Give the extent of all Plasmodium falciparum-infected red blood cells.
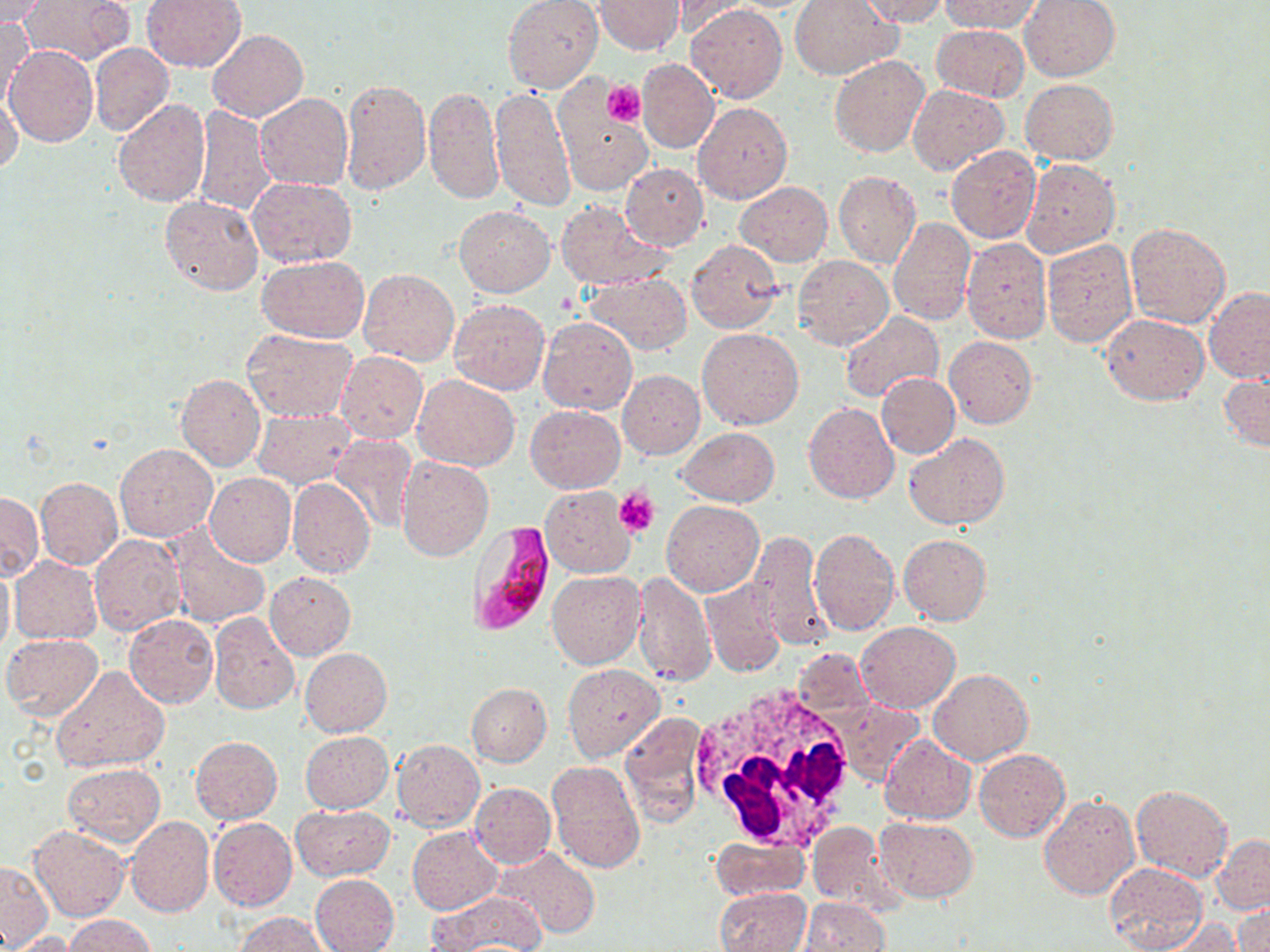
Approximate bounding boxes as (x1,y1)-(x2,y2) corner pairs in pixels.
Plasmodium falciparum-infected red blood cells: (466,520)-(556,636).

slide-level diagnosis = Plasmodium falciparum
white blood cell locations = approximate bounding boxes as (x1,y1)-(x2,y2) corner pairs in pixels: (690,683)-(859,855)
stain = May-Grünwald-Giemsa
uninfected red blood cell locations = approximate bounding boxes as (x1,y1)-(x2,y2) corner pairs in pixels: (21,0)-(135,65), (140,0)-(247,72), (503,0)-(603,93), (594,0)-(685,54), (789,0)-(900,79), (854,0)-(949,25), (941,0)-(1043,33), (1020,0)-(1120,81), (0,1)-(51,27), (669,2)-(747,39), (686,4)-(787,103), (0,18)-(34,110), (930,25)-(1029,102), (208,29)-(308,122), (90,42)-(174,137), (4,45)-(99,148), (830,54)-(928,157), (637,59)-(719,153), (1021,78)-(1118,165), (341,79)-(431,195), (490,85)-(576,211), (909,85)-(1010,174), (424,86)-(502,205), (0,91)-(22,170), (255,93)-(353,191), (113,98)-(211,207), (557,102)-(651,195), (693,102)-(792,204), (195,105)-(274,216), (945,147)-(1042,244), (1023,158)-(1121,259), (621,163)-(709,250), (834,171)-(921,269), (247,177)-(357,268), (736,181)-(833,267), (160,195)-(263,296), (556,200)-(669,289), (453,205)-(555,296), (888,217)-(977,324), (1125,222)-(1231,329), (961,238)-(1050,343), (687,239)-(784,333), (1041,239)-(1136,345), (257,254)-(370,341), (795,255)-(893,349), (358,269)-(459,365), (583,273)-(691,354), (1204,287)-(1270,384), (448,298)-(550,394), (839,311)-(943,405), (1101,313)-(1207,405), (539,317)-(637,415), (698,327)-(803,429), (244,328)-(356,422), (945,337)-(1037,429), (335,352)-(427,443), (618,370)-(705,459), (876,372)-(959,459), (1219,373)-(1270,454), (175,374)-(264,472), (412,374)-(520,471), (804,402)-(898,504), (526,405)-(624,492), (252,409)-(356,487), (676,427)-(778,505), (904,433)-(1011,529), (328,434)-(416,534), (115,444)-(217,542), (396,456)-(493,560), (204,473)-(296,567), (35,477)-(123,569), (287,477)-(374,577), (540,485)-(636,577), (0,491)-(42,580), (662,500)-(765,596), (809,526)-(899,636), (165,528)-(270,629), (748,531)-(831,650), (89,532)-(185,635), (899,533)-(992,625), (10,556)-(102,644), (0,561)-(14,664), (264,571)-(356,660), (548,571)-(645,669), (633,573)-(715,685), (702,580)-(785,678), (208,612)-(300,715), (125,614)-(217,707), (856,622)-(960,712), (1,634)-(104,721), (299,647)-(391,737), (562,663)-(664,762), (50,666)-(169,775), (928,669)-(1033,765), (467,683)-(552,766), (833,698)-(924,784), (620,713)-(709,826), (299,731)-(392,813), (881,735)-(976,823), (191,737)-(282,823), (391,738)-(484,832), (975,749)-(1070,842), (547,762)-(645,873), (62,764)-(166,847), (469,782)-(556,868), (1131,783)-(1232,882), (1039,795)-(1139,899), (291,805)-(394,881), (125,816)-(214,917), (875,816)-(978,902), (208,817)-(297,910), (807,821)-(906,915), (29,825)-(130,922), (407,826)-(502,914), (1212,835)-(1269,914), (711,836)-(809,900), (495,848)-(599,938), (1,860)-(54,948), (1104,862)-(1207,952), (310,873)-(399,952), (716,888)-(811,951), (430,893)-(544,949), (796,898)-(890,950), (1118,902)-(1233,952), (1234,902)-(1268,952), (63,914)-(156,951), (237,914)-(329,952), (1151,917)-(1245,952), (9,931)-(77,952)
field of view = single
image size = 1270×952 pixels
modality = optical microscopy
preparation = thin blood smear
platelet locations = approximate bounding boxes as (x1,y1)-(x2,y2) corner pairs in pixels: (601,79)-(646,127), (614,488)-(659,538)
magnification = 1000x